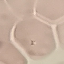

Malaria status: uninfected. Giemsa stain. Thin blood film. Automatically extracted cell patch, resized to 64 × 64 pixels. Photographed with a smartphone camera at the microscope eyepiece.